Report the malaria status.
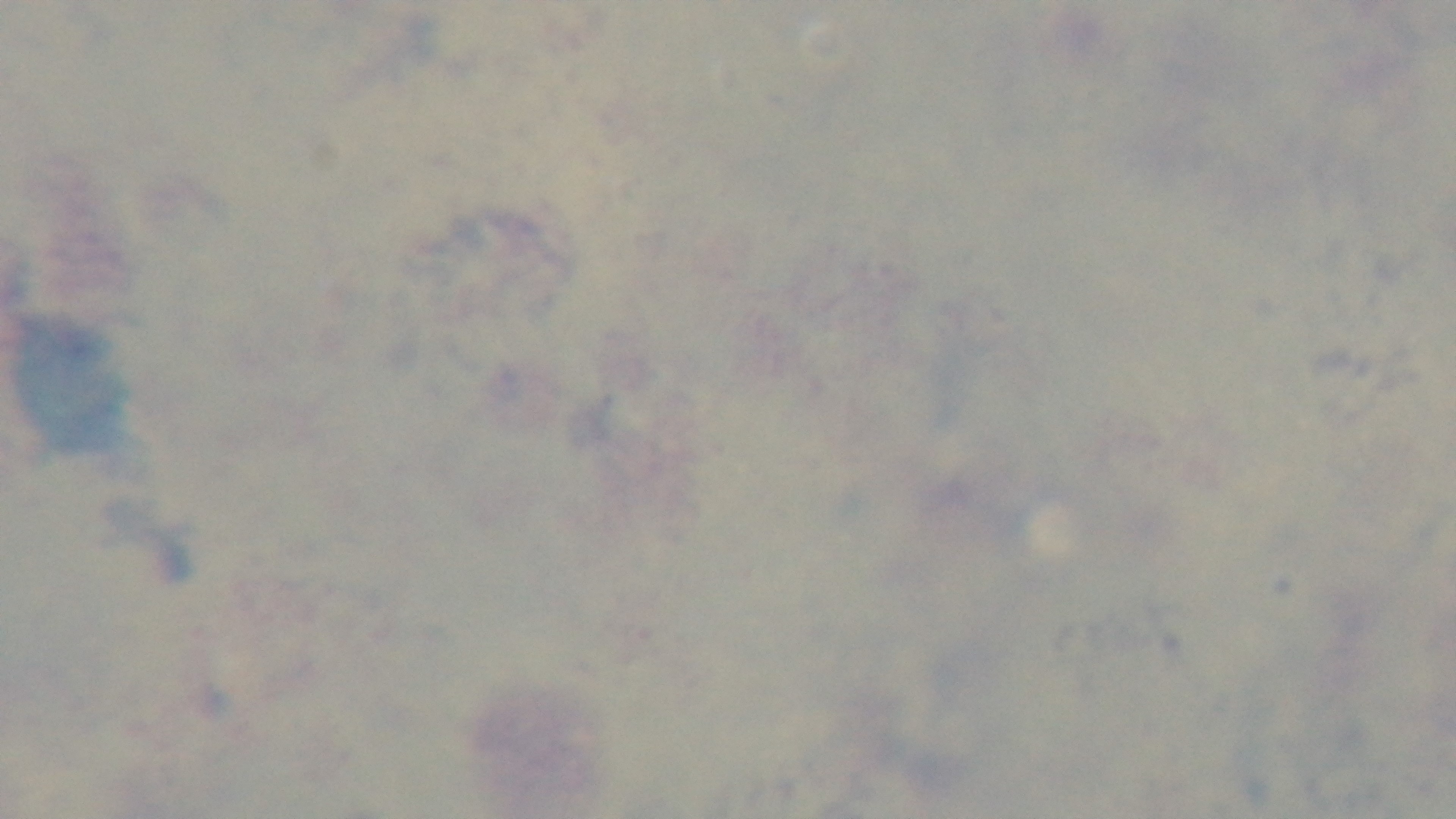

Uninfected.

Summary:
  - Preparation: thick
  - Capture: mounted 4K digital camera
  - Stain: Giemsa
  - Modality: light microscopy
  - Field of view: one from the slide
  - Objective: 100x oil immersion